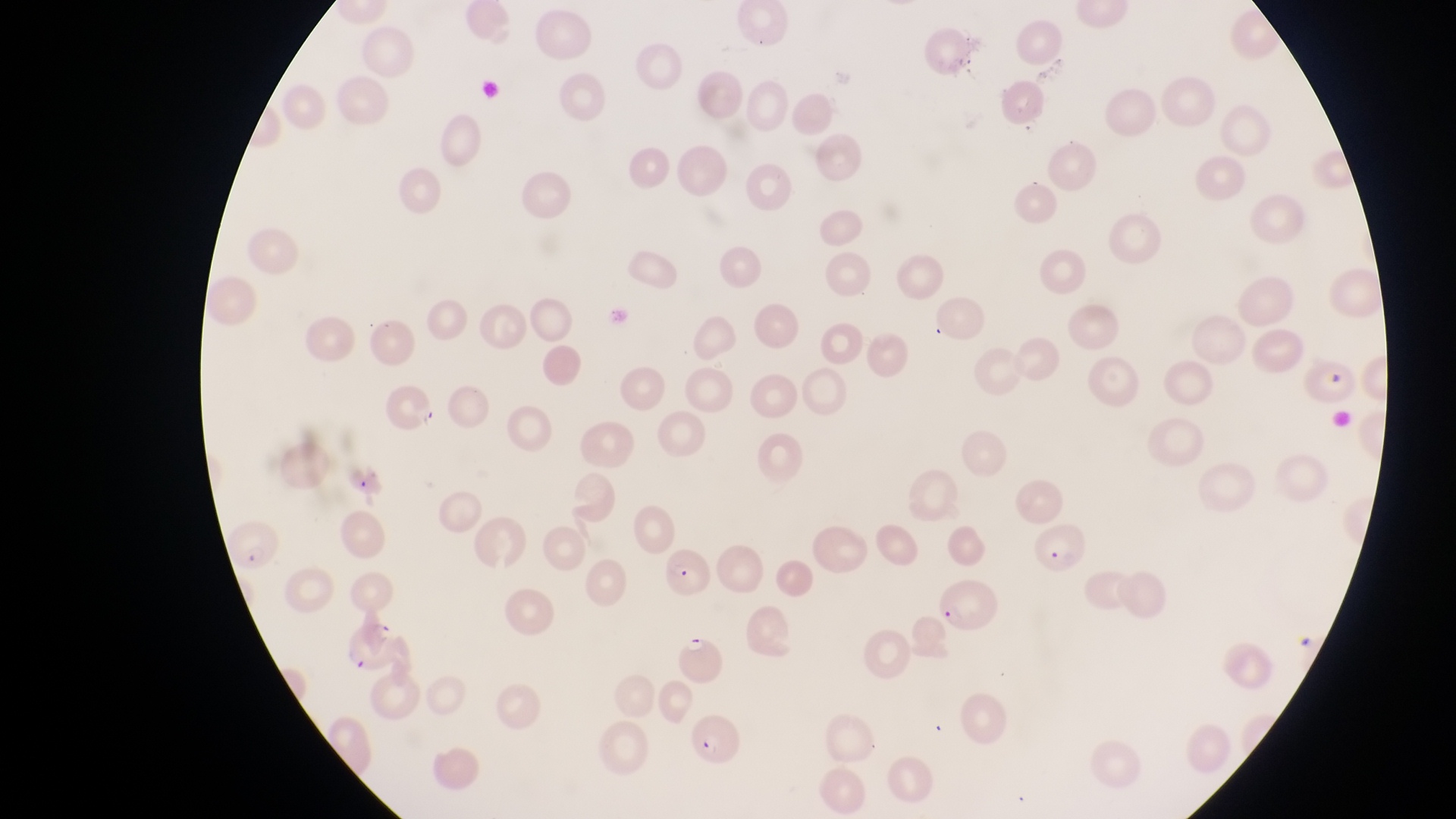

field of view = single
capture = smartphone photograph through the eyepiece of an Olympus CX-23 microscope
country = Uganda
parasitised red blood cell locations = approximate bounding boxes as [left, top, right, bottom] in pixels: [384, 383, 439, 444], [224, 518, 284, 573], [1033, 521, 1092, 580], [663, 541, 713, 601], [934, 576, 1000, 637], [341, 613, 400, 674], [673, 634, 732, 692], [684, 708, 747, 764]
preparation = thin blood smear
image size = 1456×819 pixels
magnification = 1000x